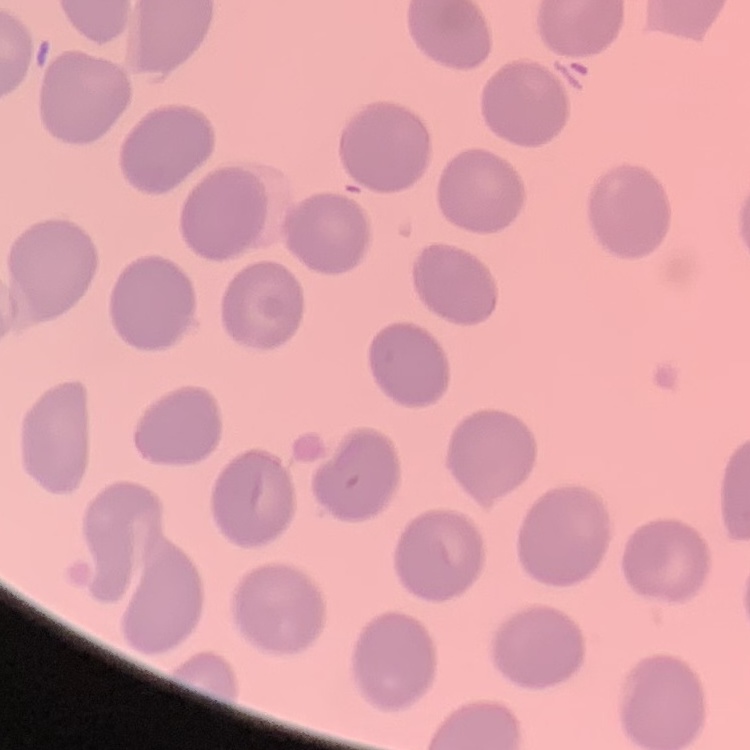
red blood cell morphology = no rouleaux formation
stain = Field's or Giemsa
image type = square crop of a larger photomicrograph
preparation = thin blood smear